Report the malaria status of this cell.
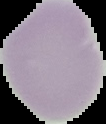
Uninfected.

Summary:
  - Preparation: thin blood smear
  - Image size: 106×124 pixels
  - Image type: segmented cell region with the area outside set to black